Report the malaria status of this cell.
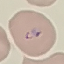
Parasitized.

capture = smartphone camera at the microscope eyepiece
preparation = thin blood film
stain = Giemsa
image type = cell patch, automatically extracted from a larger field of view and resized to 64 × 64 pixels